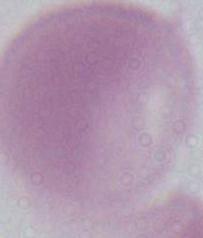

An erythrocyte is shown. Photomicrograph. Captured at 1000x magnification.